Assess this cell for malaria.
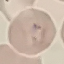

Parasitized.

Automatically extracted cell patch, resized to 64 × 64 pixels. Thin blood film. Photographed with a smartphone camera at the microscope eyepiece. Giemsa stain.